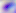 Captured at 400x magnification. Toxoplasma gondii is seen. Micrograph.